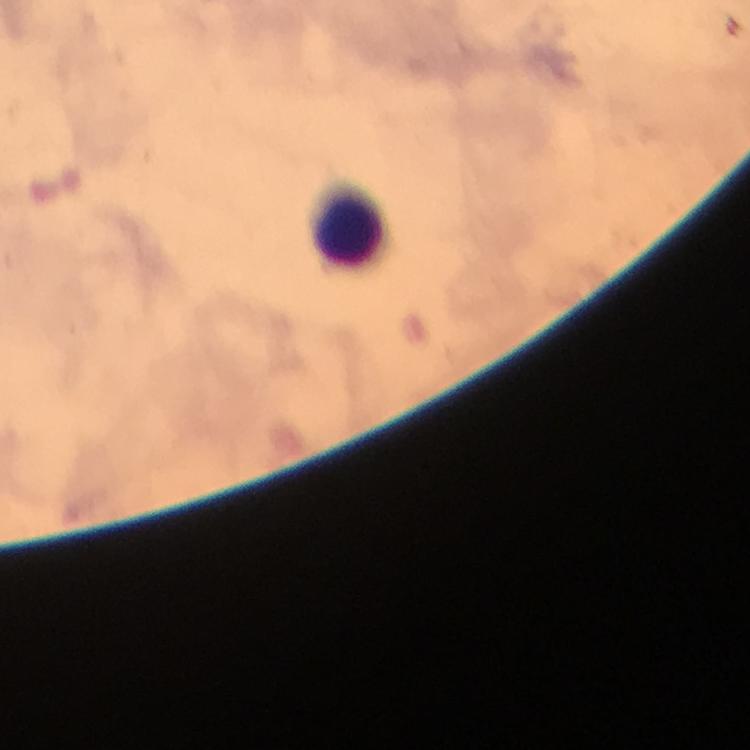

Approximate centers as (x, y) in pixels.
Summary:
  - Leukocyte locations: (348, 231)
  - Image size: 750×750 pixels
  - Malaria parasites: none seen
  - Preparation: thick blood film
  - Cropped from: a single field of view
  - Magnification: 100x
  - Context: from a diagnostic examination for malaria
  - Capture: smartphone mounted on the microscope
  - Stain: Giemsa
  - Immersion oil: used